Assess this cell for malaria.
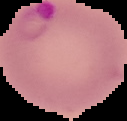
It is parasitized.

Image is 127×121 pixels. From a thin blood smear. The area outside the segmented cell region is set to black.